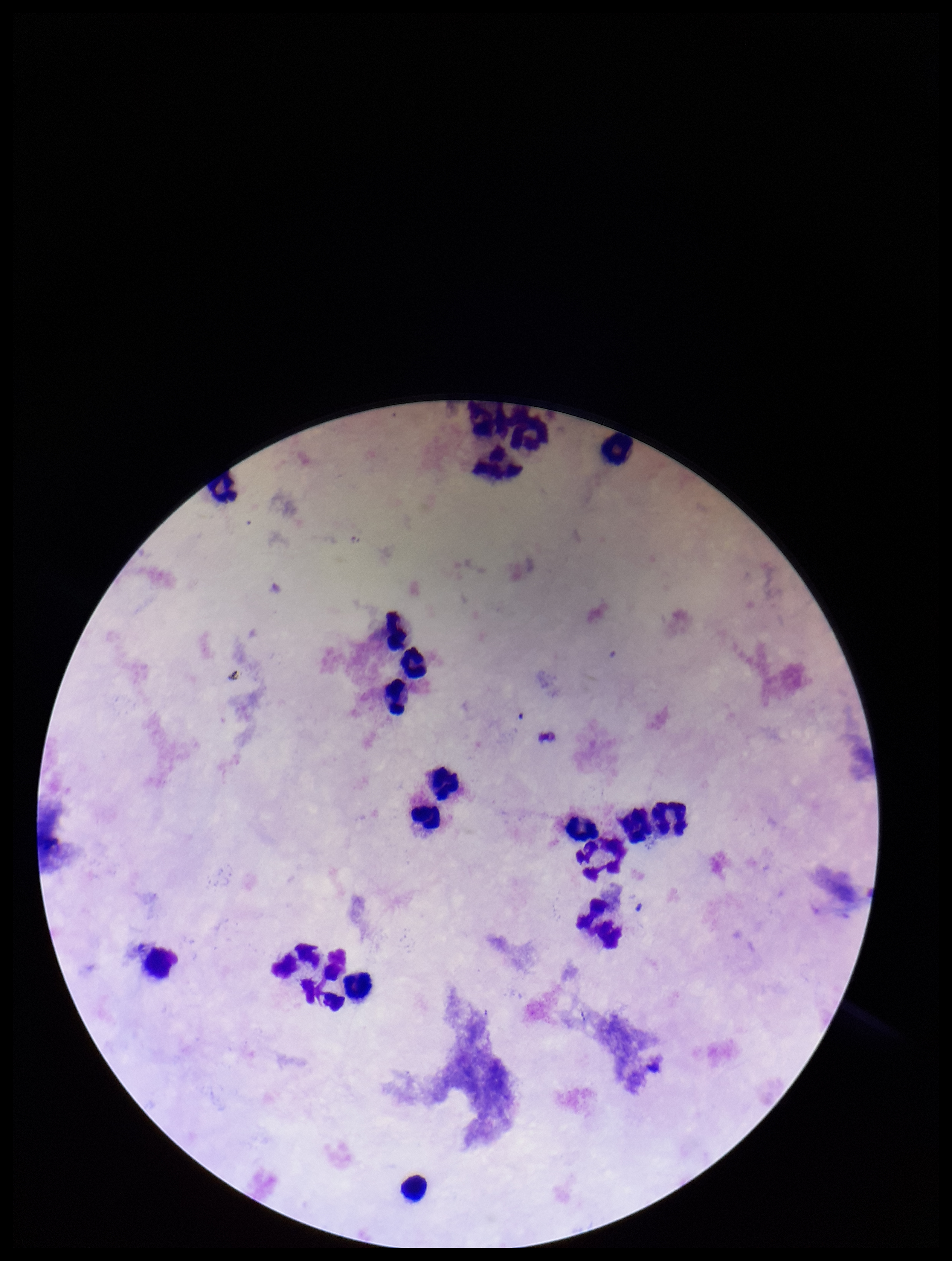

Photographed through the microscope eyepiece with a smartphone camera. Image is 952×1261 pixels. Plasmodium parasites: none identified. One field from this slide. Leukocyte count: 20. Parasite count: 0. Patient malaria status: negative. Giemsa stain. Preparation: thick smear.